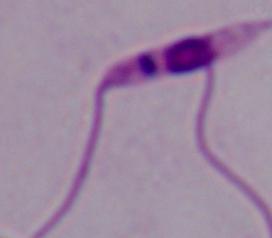

A Leishmania parasite is seen. Captured at 1000x magnification. Photomicrograph.